Report the malaria status of this cell.
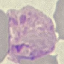

It is parasitized.

Summary:
  - Preparation: thin blood film
  - Image type: automatically extracted cell patch, resized to 64 × 64 pixels
  - Stain: Giemsa
  - Capture: smartphone camera at the microscope eyepiece